Identify the blood parasite species.
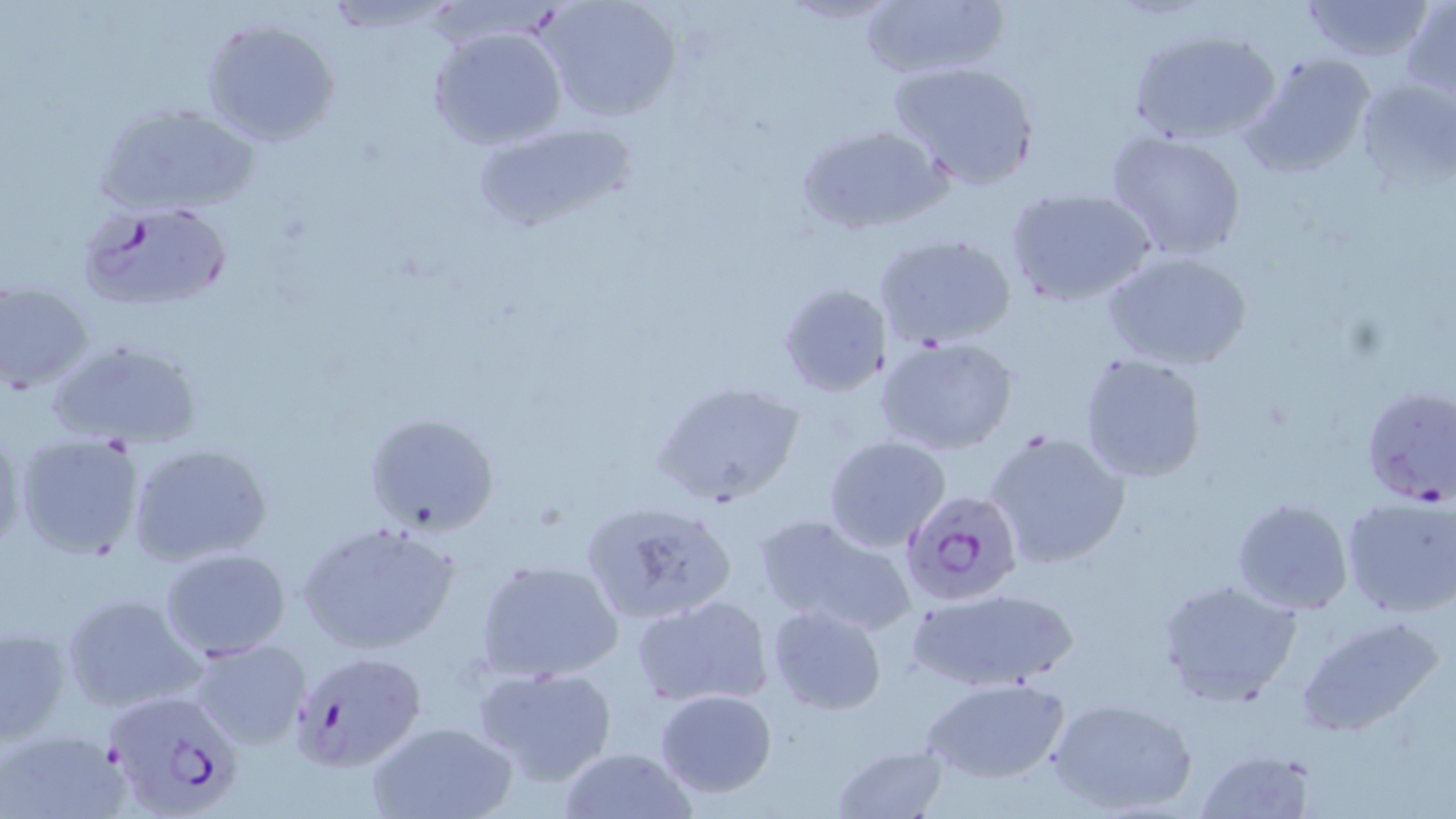

Plasmodium falciparum.

Summary:
  - Coordinate format: approximate bounding boxes as (x1, y1, x2, y2) in pixels
  - Uninfected red blood cell locations: (538, 0, 682, 124), (860, 0, 1011, 81), (1294, 0, 1437, 64), (1403, 1, 1456, 102), (200, 16, 342, 148), (426, 24, 570, 150), (1127, 25, 1284, 147), (1240, 52, 1377, 181), (886, 59, 1042, 192), (1355, 77, 1456, 187), (93, 99, 263, 216), (793, 122, 953, 236), (470, 123, 638, 233), (1102, 129, 1249, 262), (1004, 188, 1156, 308), (872, 233, 1019, 353), (1100, 248, 1253, 373), (1, 281, 92, 396), (776, 283, 892, 399), (875, 336, 1020, 456), (46, 338, 205, 451), (1078, 353, 1209, 484), (650, 379, 805, 507), (362, 412, 498, 536), (0, 421, 26, 555), (984, 429, 1133, 572), (14, 432, 146, 561), (824, 436, 951, 553), (130, 445, 272, 566), (1231, 496, 1354, 616), (1342, 496, 1456, 617), (579, 497, 738, 628), (754, 512, 921, 639), (296, 521, 461, 656), (160, 548, 291, 660), (475, 557, 624, 683), (1156, 577, 1300, 707), (904, 586, 1083, 694), (59, 591, 206, 716), (632, 595, 773, 709), (766, 603, 887, 716), (1295, 614, 1445, 736), (1, 623, 72, 745), (189, 638, 313, 751), (470, 663, 621, 789), (919, 677, 1070, 784), (654, 688, 778, 799), (1045, 697, 1198, 816), (368, 719, 519, 819), (2, 727, 131, 819), (830, 743, 952, 819), (555, 747, 696, 819), (1195, 748, 1317, 819)
  - Plasmodium falciparum-infected red blood cell locations: (77, 200, 231, 312), (1356, 383, 1456, 509), (900, 489, 1024, 608), (290, 649, 426, 772), (102, 690, 243, 819)
  - Modality: optical microscopy
  - Stain: May-Grünwald-Giemsa
  - Image size: 1456×819 pixels
  - Preparation: thin blood smear
  - Field of view: one of a larger specimen
  - Magnification: 1000x